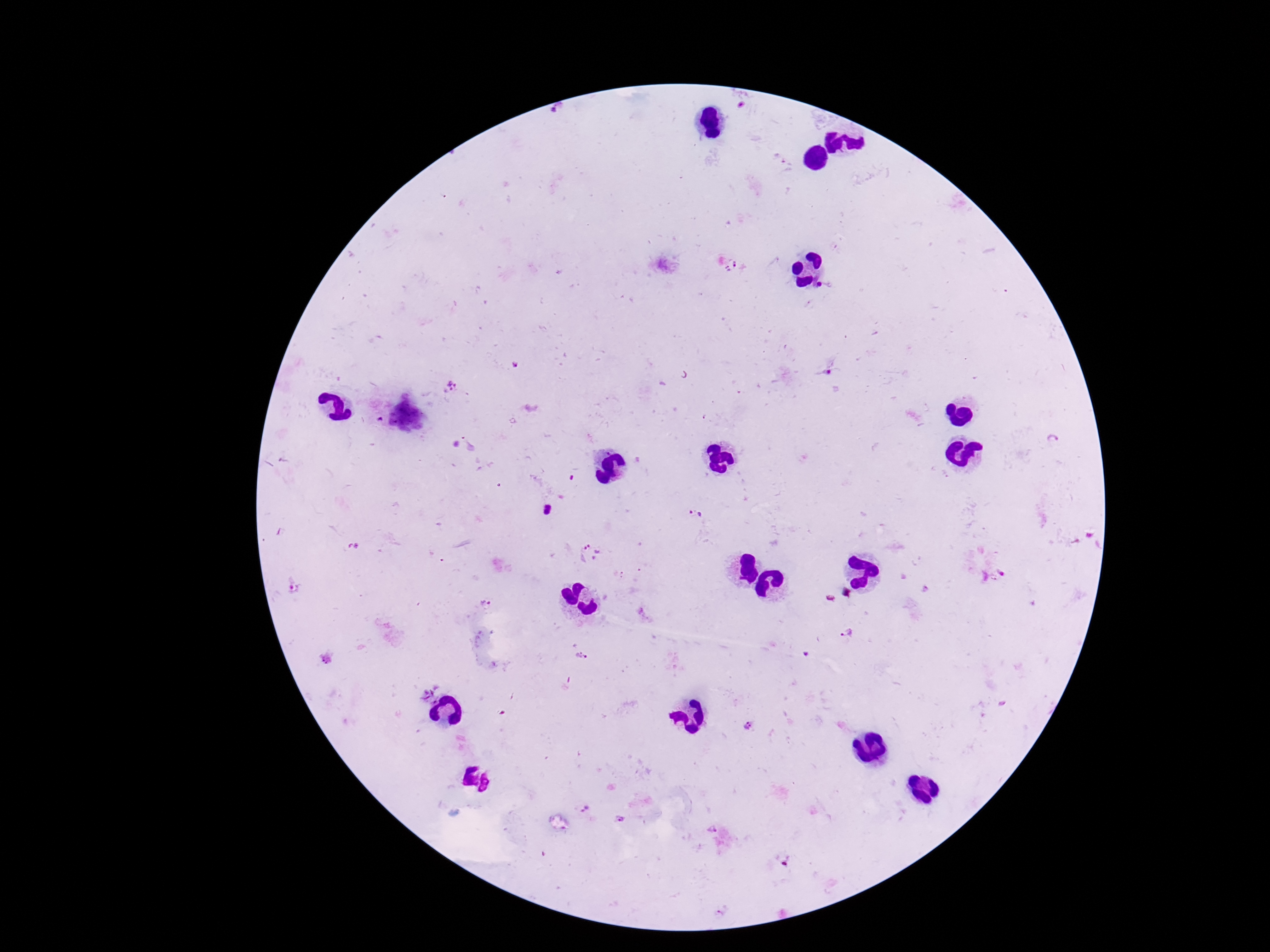
patient malaria status = infected
magnification = 100x
preparation = thick blood smear
image size = 1270×952 pixels
stain = Giemsa
field of view = single
Plasmodium parasite locations = approximate centers as (x, y) in pixels: (824, 373), (453, 391), (1052, 443), (695, 512), (590, 551), (485, 605), (844, 632), (582, 656), (748, 727), (586, 809), (620, 819), (711, 829)
capture = smartphone camera through the microscope eyepiece